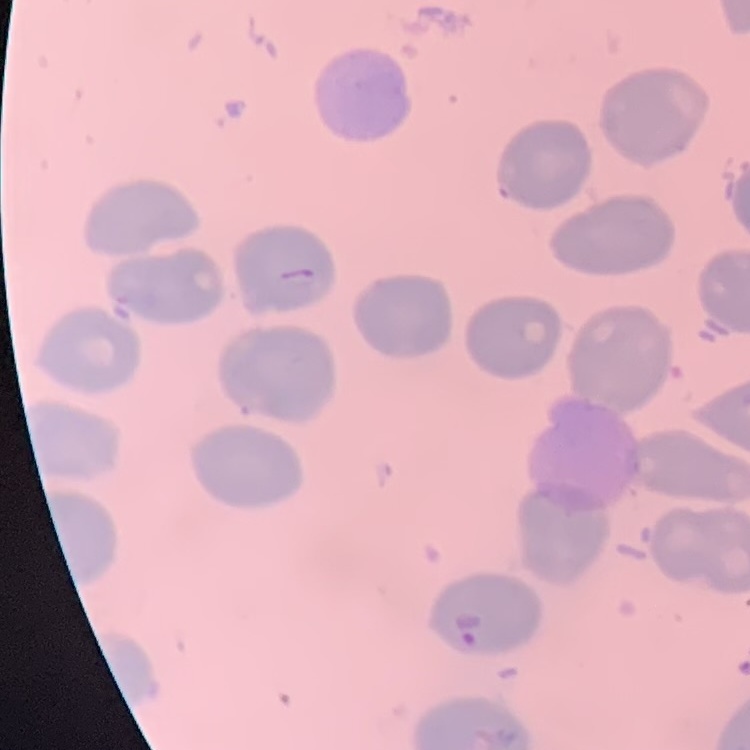
The erythrocytes show no rouleaux formation. One tile cut from a larger photomicrograph. Field's or Giemsa stain. Thin blood film.